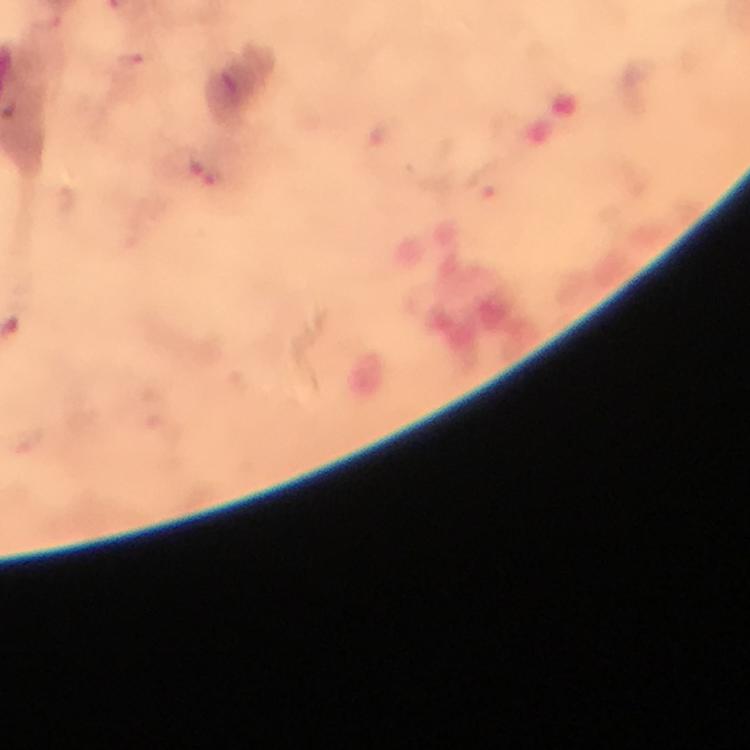
Approximate centers as {x, y} in pixels. Plasmodium parasite locations: {133, 59}, {207, 170}, {482, 184}. Image is 750×750 pixels. Giemsa stain. From a diagnostic examination for malaria. Thick smear. At 100x magnification. Cropped region of a single field of view. Immersion oil applied. Smartphone photograph taken through a microscope.